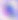 Toxoplasma gondii is shown. Micrograph. Captured at 400x magnification.